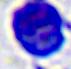
magnification = 400x
identification = leukocyte
modality = photomicrograph